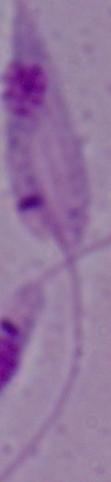
identification: Leishmania
modality: micrograph
magnification: 1000x